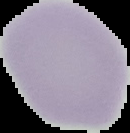
Summary:
  - Malaria status: uninfected
  - Image size: 130×133 pixels
  - Image type: segmented cell region on a black background
  - Preparation: thin blood smear